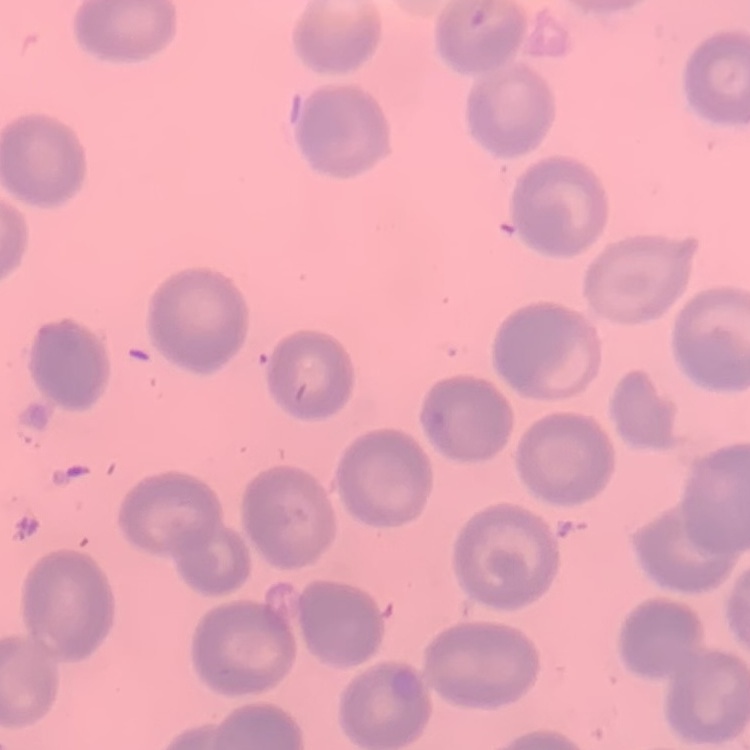
Summary:
  - Red blood cell morphology: no rouleaux formation
  - Preparation: thin blood film
  - Image type: square crop of a larger photomicrograph
  - Stain: Field's or Giemsa